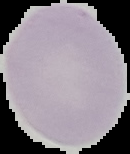

From a thin blood smear. Image is 130×154 pixels. The area outside the segmented cell region is set to black. Result: no malaria parasites detected.